Classify this cell by malaria status.
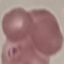

Parasitized.

image type = cell patch, automatically extracted from a larger field of view and resized to 64 × 64 pixels
capture = smartphone camera at the microscope eyepiece
preparation = thin smear
stain = Giemsa